Locate malaria parasites and leukocytes.
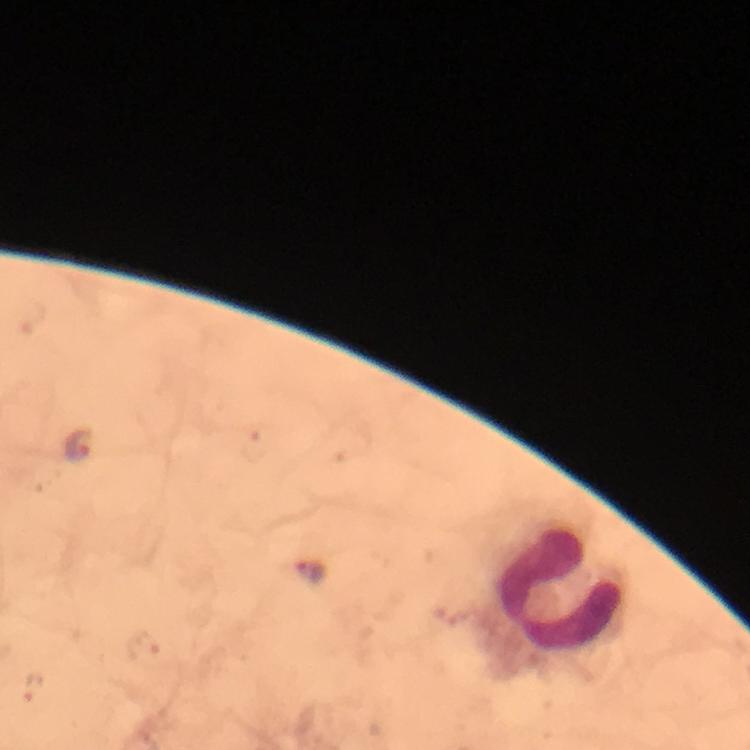
Approximate centers as {x, y} in pixels.
Malaria parasites: {79, 444}, {309, 571}, {143, 645}, {32, 688}.
Leukocytes: {560, 588}.

immersion oil = used
capture = smartphone mounted on the microscope
stain = Giemsa
context = from a diagnostic examination for malaria
cropped from = one field of view
preparation = thick blood film
image size = 750×750 pixels
magnification = 100x